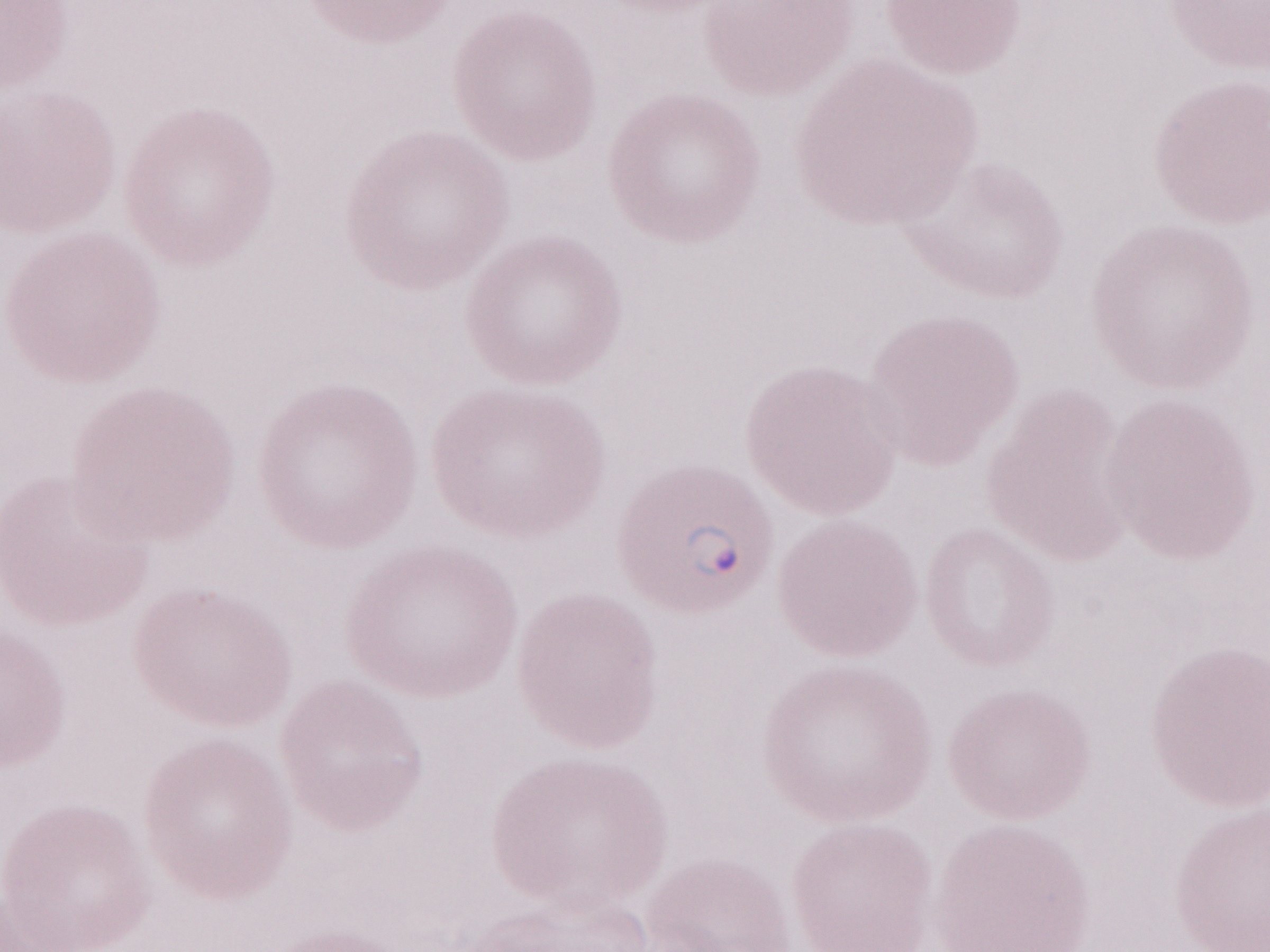

May-Grünwald-Giemsa (MGG) stain. 1,000x magnification. Olympus BX43 microscope, Olympus DP73 camera. Patient diagnosis: malaria infection. Image is 1270×952 pixels. Thin blood film. Single field of view.